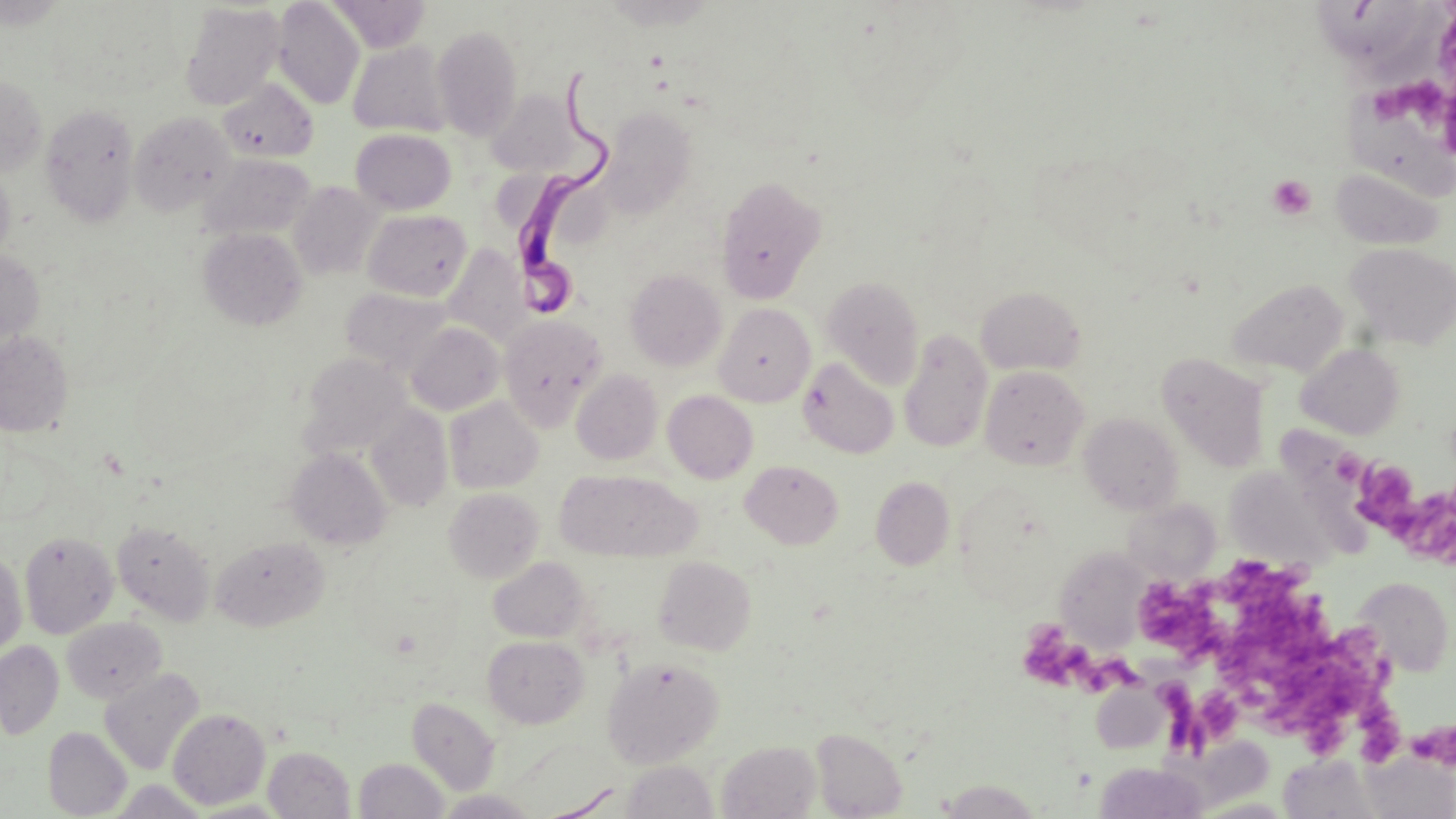

slide-level diagnosis = Trypanosoma brucei
uninfected red blood cell locations = approximate bounding boxes as (x1, y1, x2, y2) in pixels: (272, 0, 364, 109), (328, 0, 431, 52), (1317, 0, 1420, 61), (179, 2, 285, 110), (432, 24, 524, 140), (347, 40, 451, 137), (0, 75, 48, 177), (218, 77, 318, 163), (488, 90, 578, 175), (1347, 94, 1456, 196), (40, 104, 140, 226), (601, 107, 698, 212), (129, 111, 237, 217), (350, 128, 456, 214), (200, 154, 315, 240), (0, 167, 15, 265), (1330, 167, 1445, 251), (715, 175, 827, 303), (289, 181, 382, 280), (362, 208, 473, 300), (198, 227, 307, 331), (1345, 243, 1456, 351), (442, 246, 529, 345), (0, 250, 44, 349), (626, 269, 727, 371), (822, 275, 925, 388), (1226, 278, 1350, 377), (975, 285, 1086, 376), (340, 287, 453, 376), (714, 303, 815, 406), (497, 314, 606, 430), (405, 322, 505, 415), (0, 330, 74, 437), (899, 331, 993, 451), (1297, 344, 1405, 439), (300, 352, 410, 454), (1157, 353, 1270, 472), (798, 357, 899, 458), (979, 365, 1089, 470), (572, 369, 663, 464), (663, 390, 758, 484), (444, 397, 543, 494), (366, 403, 453, 512), (1078, 412, 1184, 515), (286, 448, 392, 551), (741, 460, 843, 548), (1225, 467, 1333, 570), (555, 470, 700, 562), (871, 476, 955, 570), (443, 487, 543, 583), (1123, 499, 1220, 582), (112, 521, 215, 625), (19, 531, 117, 639), (211, 536, 329, 631), (1052, 546, 1150, 649), (0, 552, 27, 656), (653, 555, 757, 655), (488, 556, 590, 643), (1353, 577, 1453, 676), (62, 617, 166, 703), (483, 635, 588, 729), (0, 641, 63, 738), (601, 656, 724, 768), (100, 668, 204, 775), (407, 696, 500, 795), (168, 708, 270, 809), (43, 727, 132, 817), (811, 728, 907, 818), (717, 740, 821, 818), (263, 746, 355, 818), (1362, 753, 1455, 818), (1278, 754, 1381, 819), (354, 757, 449, 819), (621, 760, 718, 819), (1094, 762, 1209, 819), (108, 780, 209, 818), (935, 780, 1044, 817), (435, 790, 540, 818), (1190, 796, 1298, 818)
image size = 1456×819 pixels
field of view = single
stain = May-Grünwald-Giemsa
Trypanosoma brucei locations = approximate bounding boxes as (x1, y1, x2, y2) in pixels: (505, 70, 621, 318)
magnification = 1000x
modality = optical microscopy
platelet locations = approximate bounding boxes as (x1, y1, x2, y2) in pixels: (1377, 80, 1456, 145), (1267, 174, 1316, 220), (1353, 457, 1418, 522), (1393, 490, 1455, 566), (1209, 558, 1330, 632), (1145, 581, 1232, 667), (1024, 621, 1145, 698), (1224, 624, 1404, 758), (1161, 684, 1215, 753), (1410, 722, 1455, 769)
preparation = thin blood film